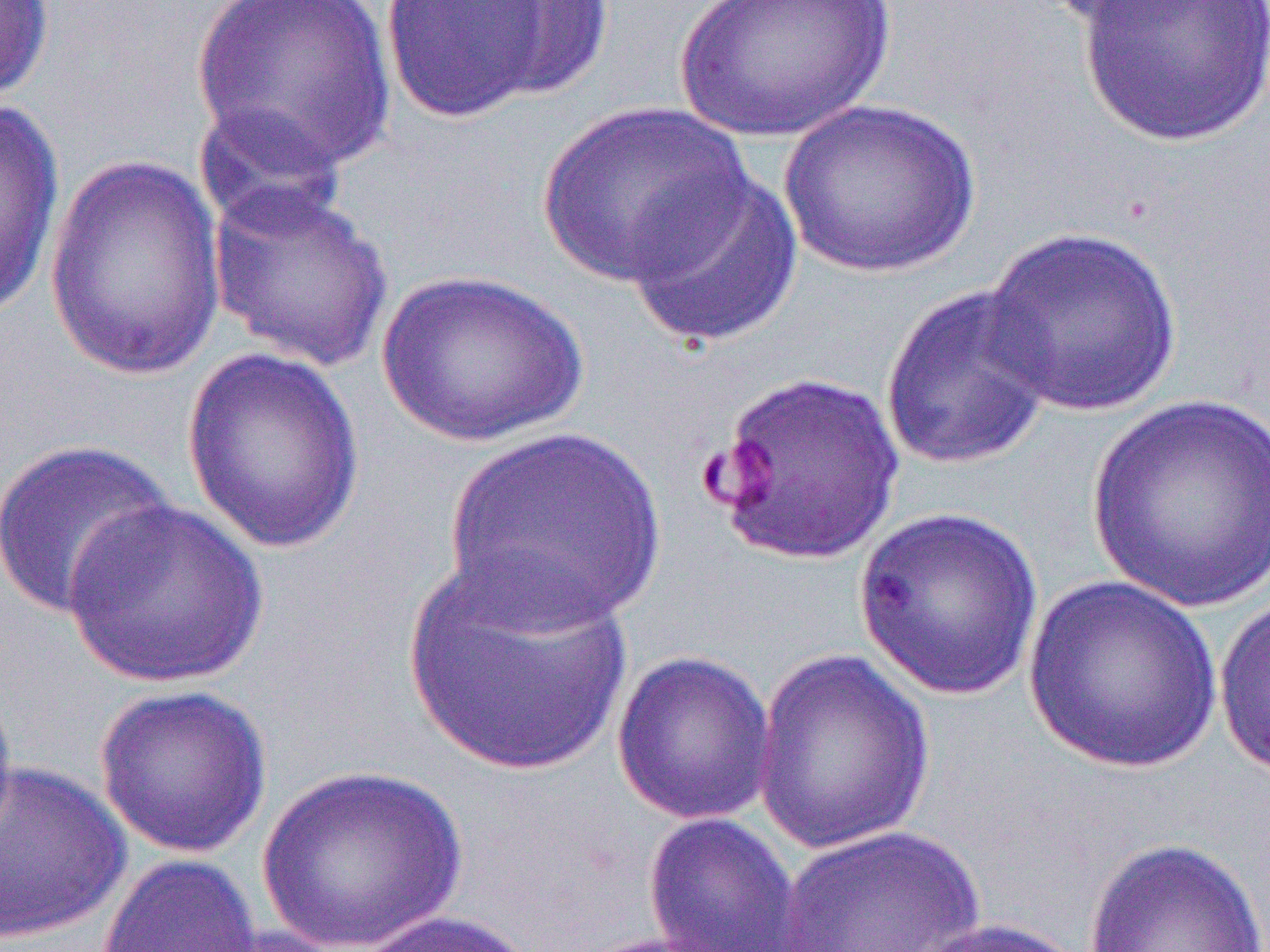
Summary:
  - Coordinate format: approximate bounding boxes as (x1,y1)-(x2,y2) corner pairs in pixels
  - Uninfected red blood cell locations: (189,0)-(398,176), (380,0)-(571,123), (462,0)-(616,104), (672,0)-(895,143), (1036,0)-(1212,28), (1076,0)-(1270,148), (0,1)-(56,108), (0,95)-(66,322), (779,99)-(981,278), (534,100)-(754,288), (192,102)-(351,240), (41,153)-(229,385), (622,166)-(804,349), (206,181)-(395,372), (981,227)-(1183,418), (375,268)-(591,448), (880,282)-(1058,473), (180,347)-(367,556), (702,369)-(906,568), (1087,392)-(1270,613), (443,426)-(666,631), (0,438)-(179,622), (61,498)-(271,689), (852,504)-(1045,703), (403,547)-(635,778), (1022,576)-(1223,774), (1213,594)-(1270,782), (611,650)-(778,825), (751,650)-(936,856), (0,676)-(18,850), (93,685)-(273,859), (0,761)-(132,945), (255,765)-(470,950), (640,812)-(807,952), (772,825)-(988,951), (1082,836)-(1268,951), (96,854)-(262,951), (350,910)-(545,952), (910,917)-(1092,952), (187,924)-(355,952)
  - Slide-level diagnosis: Plasmodium falciparum
  - Magnification: 1000x
  - Field of view: one of a larger specimen
  - Preparation: thin blood film
  - Modality: light microscopy
  - Image size: 1270×952 pixels